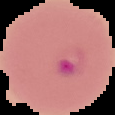
preparation = thin blood smear
malaria status = parasitized
image type = segmented cell region with the area outside set to black
image size = 115×115 pixels